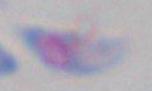

identification = Toxoplasma gondii
modality = photomicrograph
magnification = 1000x